Report the malaria status of this cell.
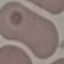
It is uninfected.

{
  "preparation": "thin smear",
  "capture": "smartphone through the microscope eyepiece",
  "image_type": "automatically extracted cell patch, resized to 64 × 64 pixels",
  "stain": "Giemsa"
}